Give the extent of all Plasmodium vivax-infected red blood cells.
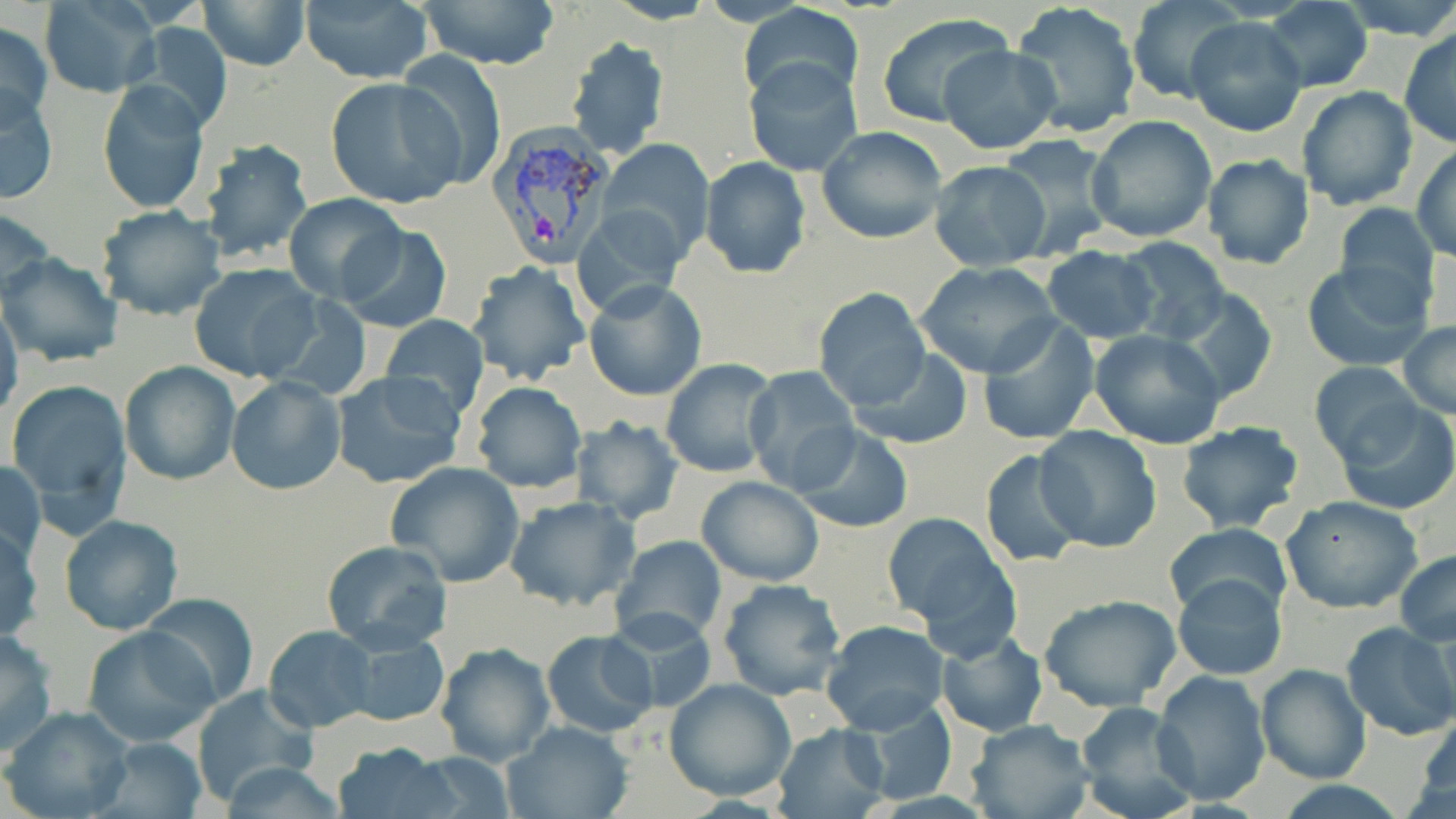

Approximate bounding boxes as [x1, y1, x2, y2] in pixels.
Plasmodium vivax-infected red blood cells: [487, 123, 621, 270].

slide-level diagnosis = Plasmodium vivax
preparation = thin blood smear
modality = optical microscopy
magnification = 1000x
uninfected red blood cell locations = approximate bounding boxes as [x1, y1, x2, y2] in pixels: [196, 0, 310, 72], [298, 0, 435, 85], [417, 0, 560, 71], [603, 0, 717, 25], [1335, 0, 1456, 40], [39, 1, 159, 97], [1128, 1, 1244, 104], [1263, 1, 1373, 92], [1010, 2, 1142, 140], [740, 4, 865, 107], [875, 13, 1017, 130], [1185, 16, 1308, 137], [0, 21, 53, 130], [126, 21, 233, 135], [1399, 26, 1456, 148], [563, 35, 671, 161], [939, 45, 1061, 155], [394, 54, 506, 192], [745, 57, 864, 177], [326, 77, 465, 210], [98, 81, 209, 215], [1295, 85, 1419, 212], [0, 88, 58, 204], [1085, 115, 1219, 243], [816, 126, 948, 244], [999, 133, 1115, 255], [200, 138, 314, 265], [598, 140, 714, 261], [1412, 143, 1456, 261], [1201, 153, 1315, 271], [699, 156, 811, 279], [929, 160, 1052, 271], [284, 193, 405, 301], [575, 203, 690, 320], [1334, 203, 1442, 312], [95, 204, 227, 321], [0, 205, 54, 304], [336, 224, 452, 334], [1114, 234, 1233, 343], [1041, 247, 1163, 343], [1, 252, 124, 367], [1303, 260, 1435, 372], [465, 261, 591, 386], [916, 262, 1064, 380], [188, 264, 322, 383], [583, 280, 707, 404], [1169, 286, 1280, 405], [811, 287, 931, 412], [0, 303, 23, 423], [380, 315, 488, 419], [976, 317, 1101, 444], [1398, 322, 1456, 420], [1090, 328, 1227, 448], [849, 348, 973, 450], [660, 358, 779, 478], [118, 361, 240, 485], [1310, 361, 1423, 469], [742, 366, 860, 493], [330, 371, 466, 489], [226, 375, 345, 495], [5, 378, 132, 517], [471, 382, 587, 494], [1333, 399, 1456, 515], [569, 415, 685, 524], [1174, 419, 1306, 535], [790, 425, 915, 533], [1034, 425, 1163, 553], [979, 448, 1089, 569], [2, 459, 45, 564], [385, 461, 525, 588], [695, 476, 824, 586], [1280, 494, 1424, 614], [503, 495, 639, 614], [881, 513, 1019, 655], [59, 515, 184, 635], [1, 524, 43, 645], [1164, 524, 1292, 623], [610, 536, 728, 647], [319, 540, 453, 653], [1394, 548, 1456, 646], [1171, 573, 1288, 681], [717, 578, 848, 701], [140, 593, 257, 708], [1039, 595, 1181, 712], [607, 610, 717, 716], [820, 620, 948, 735], [1340, 620, 1456, 743], [81, 625, 218, 746], [263, 625, 378, 732], [934, 627, 1048, 736], [0, 629, 58, 758], [338, 629, 451, 729], [542, 629, 658, 738], [435, 643, 555, 766], [1257, 664, 1371, 783], [1152, 670, 1272, 807], [664, 676, 796, 802], [190, 686, 318, 805], [842, 697, 961, 803], [1075, 701, 1197, 819], [3, 706, 134, 819], [1414, 707, 1456, 814], [965, 719, 1094, 819], [502, 720, 635, 819], [772, 724, 891, 819], [91, 736, 209, 819], [329, 741, 458, 819], [404, 751, 514, 816], [215, 762, 353, 818]
field of view = single
stain = May-Grünwald-Giemsa
image size = 1456×819 pixels